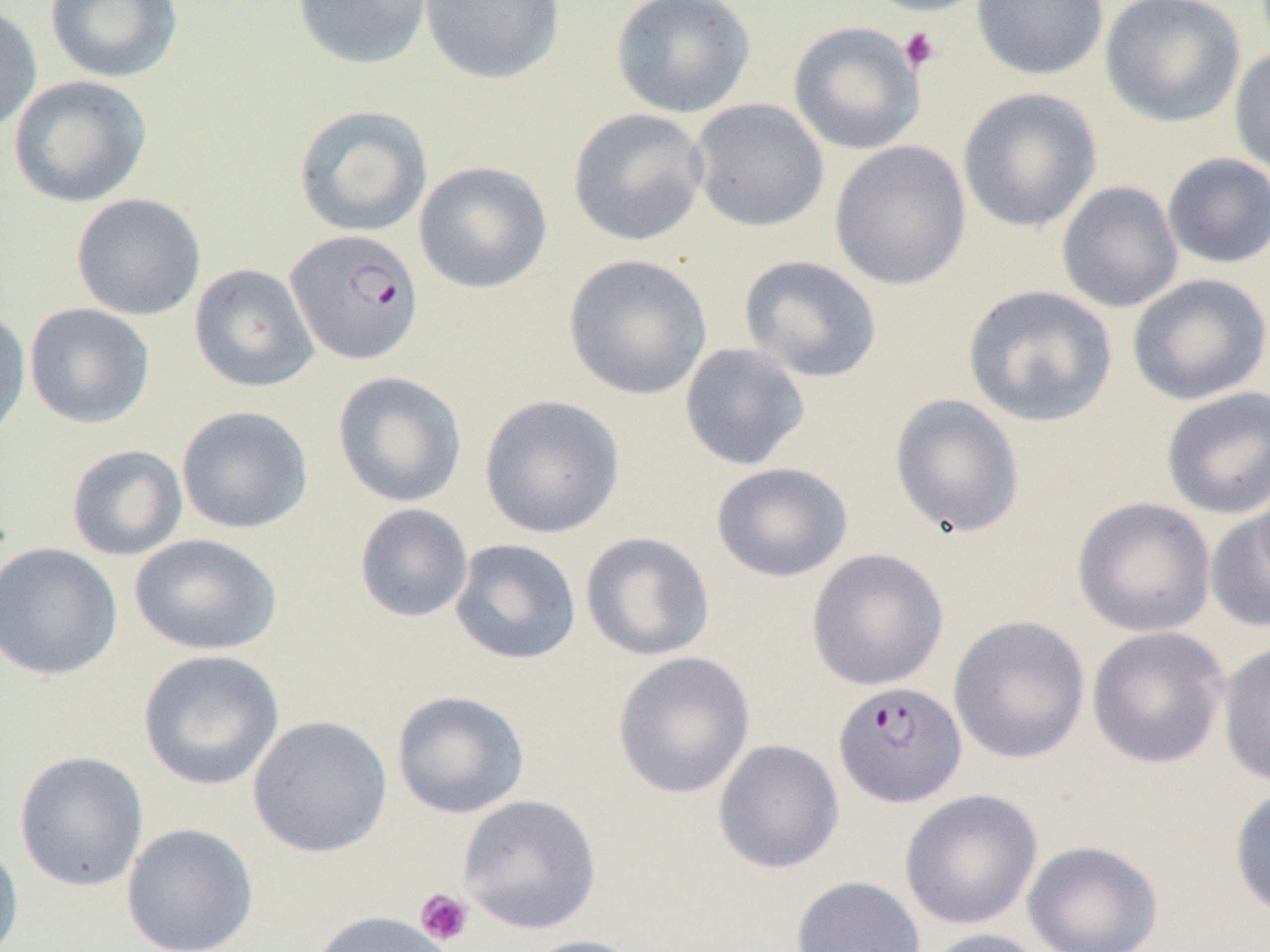

{
  "slide_level_diagnosis": "Plasmodium falciparum",
  "modality": "light microscopy",
  "image_size": "1270×952 pixels",
  "uninfected_red_blood_cell_locations": "approximate bounding boxes as (x1,y1)-(x2,y2) corner pairs in pixels: (45,0)-(184,84), (292,0)-(433,70), (419,0)-(565,85), (610,0)-(756,119), (857,0)-(994,17), (971,0)-(1108,80), (1099,0)-(1246,128), (0,3)-(42,135), (787,21)-(925,155), (1229,45)-(1270,178), (8,75)-(152,208), (957,87)-(1102,233), (689,98)-(829,232), (294,105)-(433,238), (568,108)-(710,247), (829,140)-(971,291), (1162,153)-(1270,269), (413,161)-(552,294), (1057,181)-(1184,313), (70,193)-(206,321), (563,254)-(713,401), (738,254)-(882,383), (189,263)-(319,392), (1127,273)-(1270,405), (962,284)-(1117,427), (24,303)-(155,429), (0,307)-(31,444), (679,342)-(811,471), (332,371)-(467,508), (1160,386)-(1270,520), (479,394)-(625,539), (889,394)-(1025,539), (176,405)-(313,535), (65,444)-(188,561), (710,462)-(853,583), (1072,497)-(1216,637), (353,503)-(473,623), (1204,508)-(1270,633), (580,531)-(715,662), (129,533)-(282,656), (449,538)-(582,665), (0,541)-(122,681), (806,548)-(949,691), (948,615)-(1090,764), (1086,626)-(1229,769), (1217,641)-(1270,787), (137,649)-(284,790), (612,651)-(756,799), (391,690)-(530,819), (248,715)-(393,858), (713,739)-(845,874), (14,750)-(149,892), (1228,785)-(1270,919), (900,789)-(1043,930), (457,794)-(601,934), (121,823)-(259,952), (0,837)-(24,952), (1023,840)-(1163,952), (790,875)-(926,952), (309,910)-(458,952), (920,928)-(1050,952), (517,934)-(649,952)",
  "platelet_locations": "approximate bounding boxes as (x1,y1)-(x2,y2) corner pairs in pixels: (899,27)-(940,74), (415,888)-(474,947)",
  "field_of_view": "single",
  "magnification": "1000x",
  "plasmodium_falciparum_infected_red_blood_cell_locations": "approximate bounding boxes as (x1,y1)-(x2,y2) corner pairs in pixels: (285,228)-(424,365), (833,681)-(967,808)",
  "preparation": "thin blood film"
}